Assess the morphology of the erythrocytes.
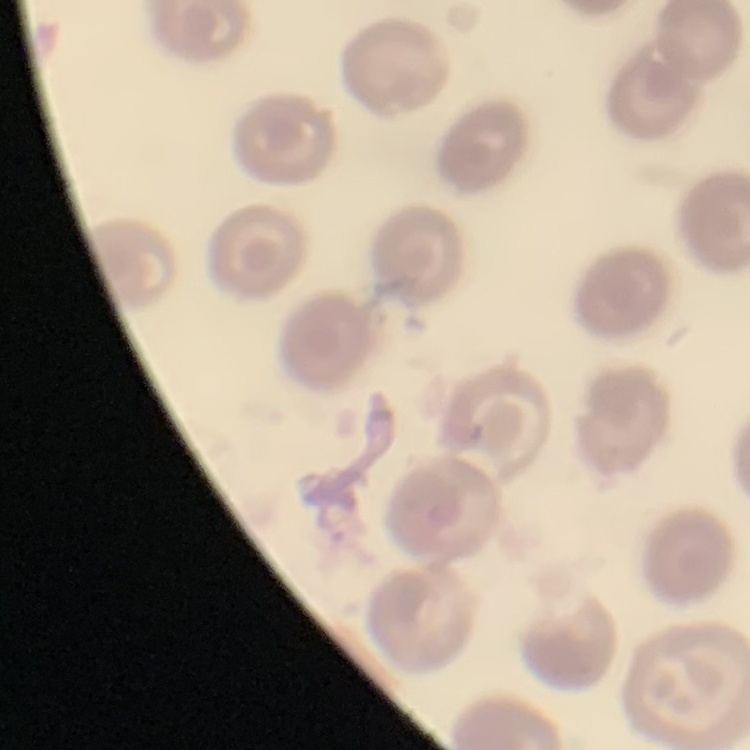
They show no rouleaux formation.

stain = Field's or Giemsa
preparation = thin blood film
image type = square crop of a larger photomicrograph